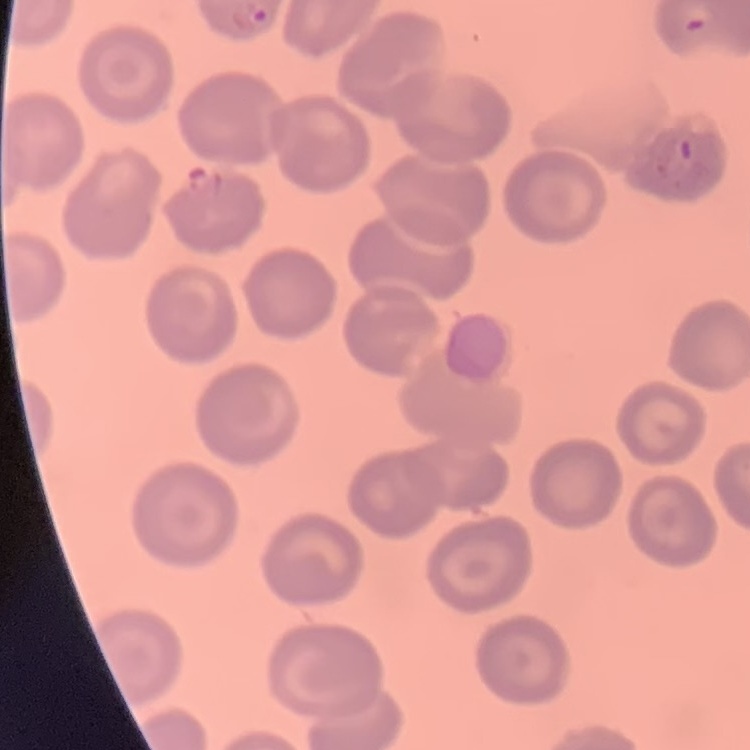

erythrocyte morphology = no rouleaux formation
image type = one tile cut from a larger photomicrograph
stain = Field's or Giemsa
preparation = thin blood film